Assess this cell for malaria.
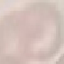
It is uninfected.

Summary:
  - Image type: automatically extracted cell patch, resized to 64 × 64 pixels
  - Preparation: thin smear
  - Stain: Giemsa
  - Capture: smartphone through the microscope eyepiece